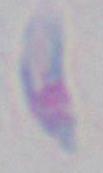

Captured at 1000x magnification. Photomicrograph. Toxoplasma gondii is seen.